Classify this cell by malaria status.
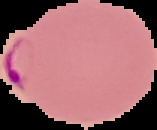
It is parasitized.

From a thin blood smear. Image is 157×130 pixels. Segmented cell region on a black background.